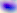

modality: micrograph
identification: Toxoplasma gondii
magnification: 400x